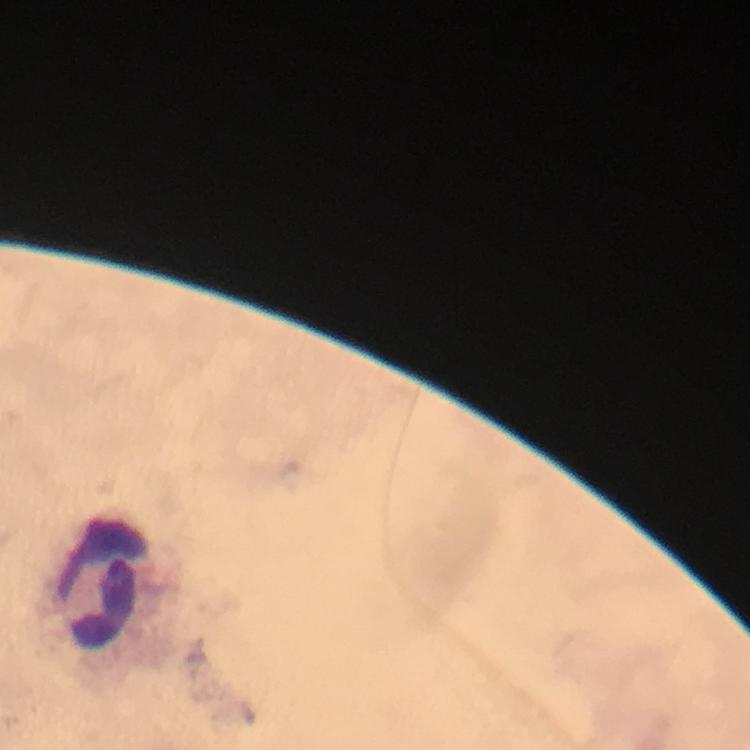

{
  "malaria_parasites": "none detected",
  "context": "from a malaria diagnostic workup",
  "stain": "Giemsa",
  "leukocyte_locations": "approximate centers as {x, y} in pixels: {103, 583}",
  "cropped_from": "a single field of view",
  "magnification": "100x",
  "image_size": "750×750 pixels",
  "preparation": "thick smear",
  "immersion_oil": "applied",
  "capture": "smartphone mounted on the microscope"
}